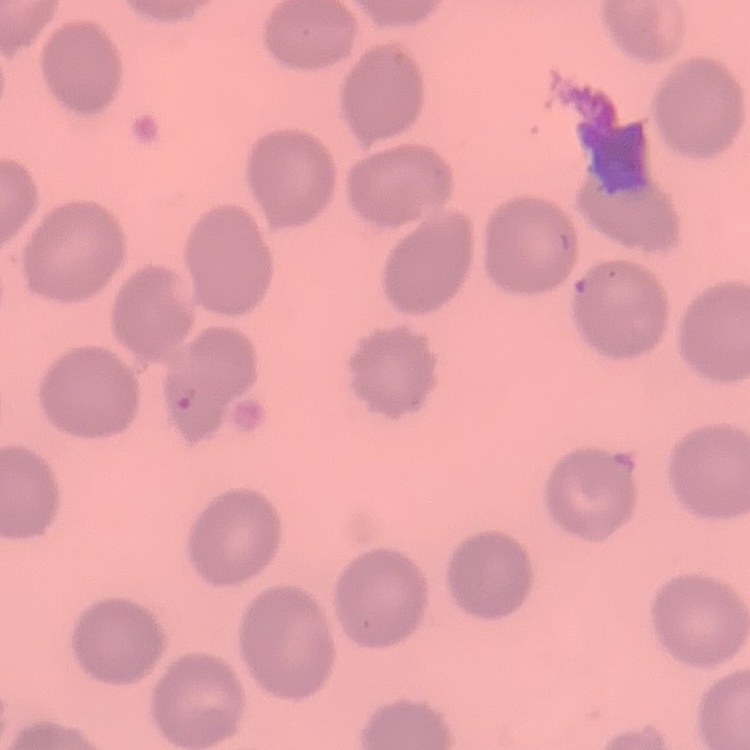
red blood cell morphology = no rouleaux formation
preparation = thin blood smear
stain = Field's or Giemsa
image type = one tile cut from a larger photomicrograph